Outline each Plasmodium falciparum-infected red blood cell.
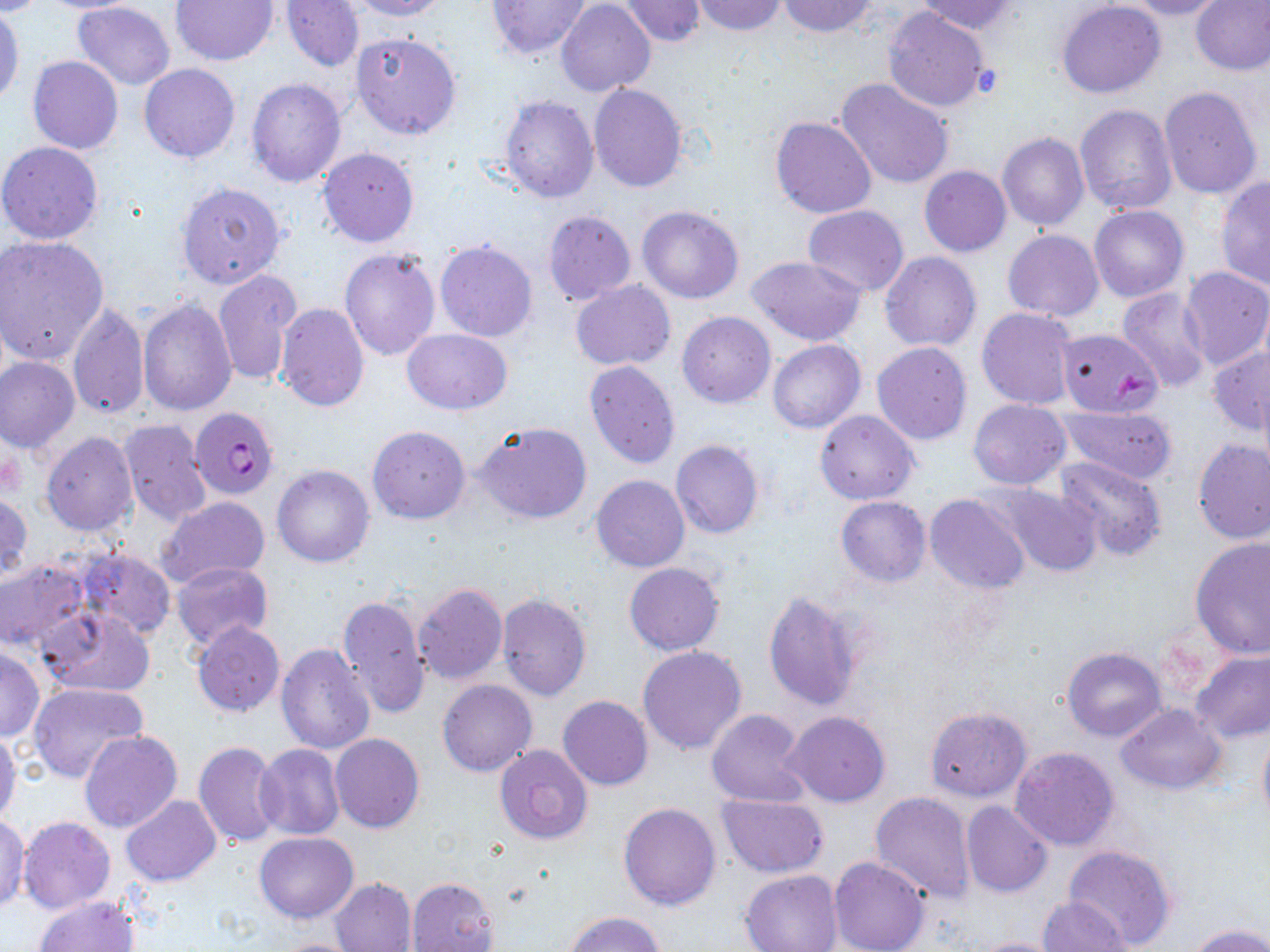

Approximate bounding boxes as named x1/y1/x2/y2 corners in pixels.
Plasmodium falciparum-infected red blood cells: (x1=190, y1=407, x2=278, y2=500).

{
  "slide_level_diagnosis": "Plasmodium falciparum",
  "image_size": "1270×952 pixels",
  "platelet_locations": "approximate bounding boxes as named x1/y1/x2/y2 corners in pixels: (x1=1112, y1=369, x2=1153, y2=403)",
  "preparation": "thin blood smear",
  "stain": "May-Grünwald-Giemsa",
  "magnification": "1000x",
  "modality": "optical microscopy",
  "field_of_view": "one of a larger specimen",
  "uninfected_red_blood_cell_locations": "approximate bounding boxes as named x1/y1/x2/y2 corners in pixels: (x1=33, y1=0, x2=146, y2=13), (x1=169, y1=0, x2=279, y2=66), (x1=280, y1=0, x2=364, y2=72), (x1=350, y1=0, x2=451, y2=20), (x1=485, y1=0, x2=593, y2=59), (x1=693, y1=0, x2=787, y2=34), (x1=1119, y1=0, x2=1226, y2=20), (x1=1191, y1=0, x2=1270, y2=75), (x1=620, y1=1, x2=706, y2=45), (x1=779, y1=1, x2=876, y2=36), (x1=917, y1=1, x2=1018, y2=36), (x1=1056, y1=1, x2=1166, y2=98), (x1=71, y1=2, x2=176, y2=89), (x1=557, y1=2, x2=655, y2=97), (x1=883, y1=4, x2=992, y2=112), (x1=0, y1=5, x2=24, y2=108), (x1=351, y1=32, x2=462, y2=140), (x1=28, y1=56, x2=123, y2=154), (x1=139, y1=63, x2=240, y2=163), (x1=245, y1=76, x2=347, y2=188), (x1=834, y1=77, x2=956, y2=189), (x1=589, y1=82, x2=688, y2=193), (x1=1158, y1=85, x2=1264, y2=201), (x1=499, y1=95, x2=599, y2=203), (x1=1075, y1=104, x2=1177, y2=215), (x1=770, y1=117, x2=875, y2=219), (x1=997, y1=133, x2=1088, y2=231), (x1=0, y1=141, x2=104, y2=245), (x1=317, y1=147, x2=420, y2=248), (x1=919, y1=165, x2=1011, y2=256), (x1=1215, y1=177, x2=1270, y2=290), (x1=175, y1=181, x2=286, y2=288), (x1=637, y1=205, x2=744, y2=304), (x1=802, y1=205, x2=910, y2=296), (x1=1089, y1=205, x2=1189, y2=302), (x1=543, y1=209, x2=636, y2=305), (x1=1003, y1=229, x2=1104, y2=321), (x1=0, y1=234, x2=109, y2=365), (x1=434, y1=238, x2=539, y2=343), (x1=339, y1=247, x2=440, y2=362), (x1=879, y1=251, x2=982, y2=351), (x1=747, y1=256, x2=866, y2=346), (x1=1179, y1=265, x2=1270, y2=370), (x1=213, y1=268, x2=301, y2=386), (x1=570, y1=281, x2=676, y2=371), (x1=1116, y1=288, x2=1213, y2=391), (x1=137, y1=299, x2=236, y2=416), (x1=68, y1=302, x2=149, y2=420), (x1=275, y1=302, x2=369, y2=413), (x1=977, y1=307, x2=1078, y2=409), (x1=677, y1=311, x2=775, y2=408), (x1=402, y1=328, x2=511, y2=414), (x1=1056, y1=328, x2=1162, y2=417), (x1=768, y1=339, x2=866, y2=434), (x1=872, y1=342, x2=972, y2=444), (x1=1208, y1=345, x2=1270, y2=435), (x1=1, y1=357, x2=81, y2=453), (x1=584, y1=361, x2=681, y2=469), (x1=1257, y1=377, x2=1270, y2=486), (x1=968, y1=399, x2=1070, y2=489), (x1=1057, y1=404, x2=1180, y2=485), (x1=814, y1=409, x2=919, y2=504), (x1=118, y1=419, x2=212, y2=526), (x1=474, y1=422, x2=592, y2=523), (x1=367, y1=425, x2=471, y2=523), (x1=41, y1=432, x2=139, y2=536), (x1=1193, y1=438, x2=1270, y2=544), (x1=671, y1=439, x2=765, y2=539), (x1=1054, y1=455, x2=1167, y2=561), (x1=272, y1=464, x2=376, y2=568), (x1=590, y1=475, x2=689, y2=573), (x1=992, y1=483, x2=1102, y2=577), (x1=1, y1=491, x2=31, y2=582), (x1=925, y1=494, x2=1029, y2=595), (x1=155, y1=497, x2=271, y2=589), (x1=836, y1=497, x2=932, y2=586), (x1=1190, y1=537, x2=1270, y2=658), (x1=71, y1=547, x2=177, y2=639), (x1=0, y1=557, x2=91, y2=653), (x1=170, y1=561, x2=274, y2=652), (x1=624, y1=561, x2=724, y2=655), (x1=413, y1=583, x2=508, y2=685), (x1=497, y1=591, x2=592, y2=701), (x1=763, y1=591, x2=863, y2=712), (x1=336, y1=593, x2=431, y2=720), (x1=39, y1=606, x2=156, y2=698), (x1=191, y1=621, x2=285, y2=717), (x1=276, y1=642, x2=376, y2=755), (x1=0, y1=646, x2=44, y2=742), (x1=638, y1=646, x2=747, y2=756), (x1=1063, y1=648, x2=1166, y2=741), (x1=1191, y1=650, x2=1270, y2=743), (x1=437, y1=678, x2=537, y2=776), (x1=27, y1=683, x2=149, y2=784), (x1=558, y1=695, x2=653, y2=789), (x1=1116, y1=704, x2=1225, y2=793), (x1=925, y1=707, x2=1032, y2=801), (x1=706, y1=708, x2=810, y2=807), (x1=781, y1=712, x2=890, y2=805), (x1=1257, y1=727, x2=1270, y2=829), (x1=0, y1=730, x2=20, y2=824), (x1=79, y1=730, x2=182, y2=834), (x1=331, y1=733, x2=424, y2=833), (x1=193, y1=741, x2=284, y2=848), (x1=255, y1=744, x2=345, y2=840), (x1=494, y1=745, x2=594, y2=846), (x1=1010, y1=747, x2=1120, y2=851), (x1=869, y1=792, x2=978, y2=903), (x1=715, y1=794, x2=828, y2=878), (x1=120, y1=796, x2=220, y2=886), (x1=961, y1=800, x2=1053, y2=897), (x1=617, y1=802, x2=722, y2=911), (x1=19, y1=816, x2=115, y2=915), (x1=0, y1=817, x2=30, y2=911), (x1=255, y1=832, x2=358, y2=923), (x1=1063, y1=845, x2=1177, y2=950), (x1=829, y1=855, x2=929, y2=952), (x1=739, y1=870, x2=840, y2=952), (x1=406, y1=877, x2=499, y2=952), (x1=329, y1=878, x2=417, y2=952), (x1=35, y1=896, x2=138, y2=952), (x1=1038, y1=896, x2=1129, y2=951), (x1=565, y1=912, x2=664, y2=952), (x1=1186, y1=924, x2=1270, y2=952), (x1=967, y1=936, x2=1071, y2=952), (x1=266, y1=937, x2=369, y2=952)"
}